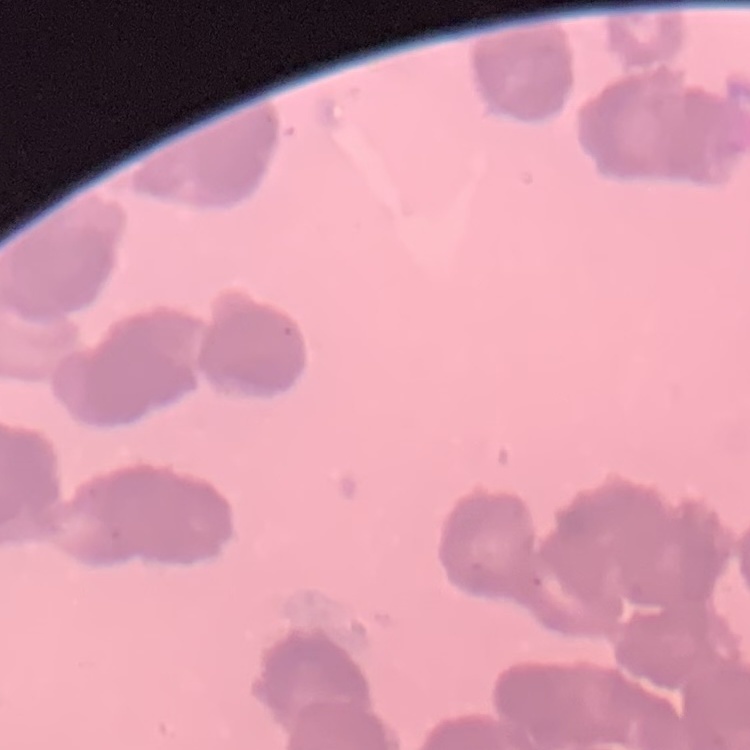 The erythrocytes show rouleaux formation. Thin blood smear. One tile cut from a larger photomicrograph. Field's or Giemsa stain.